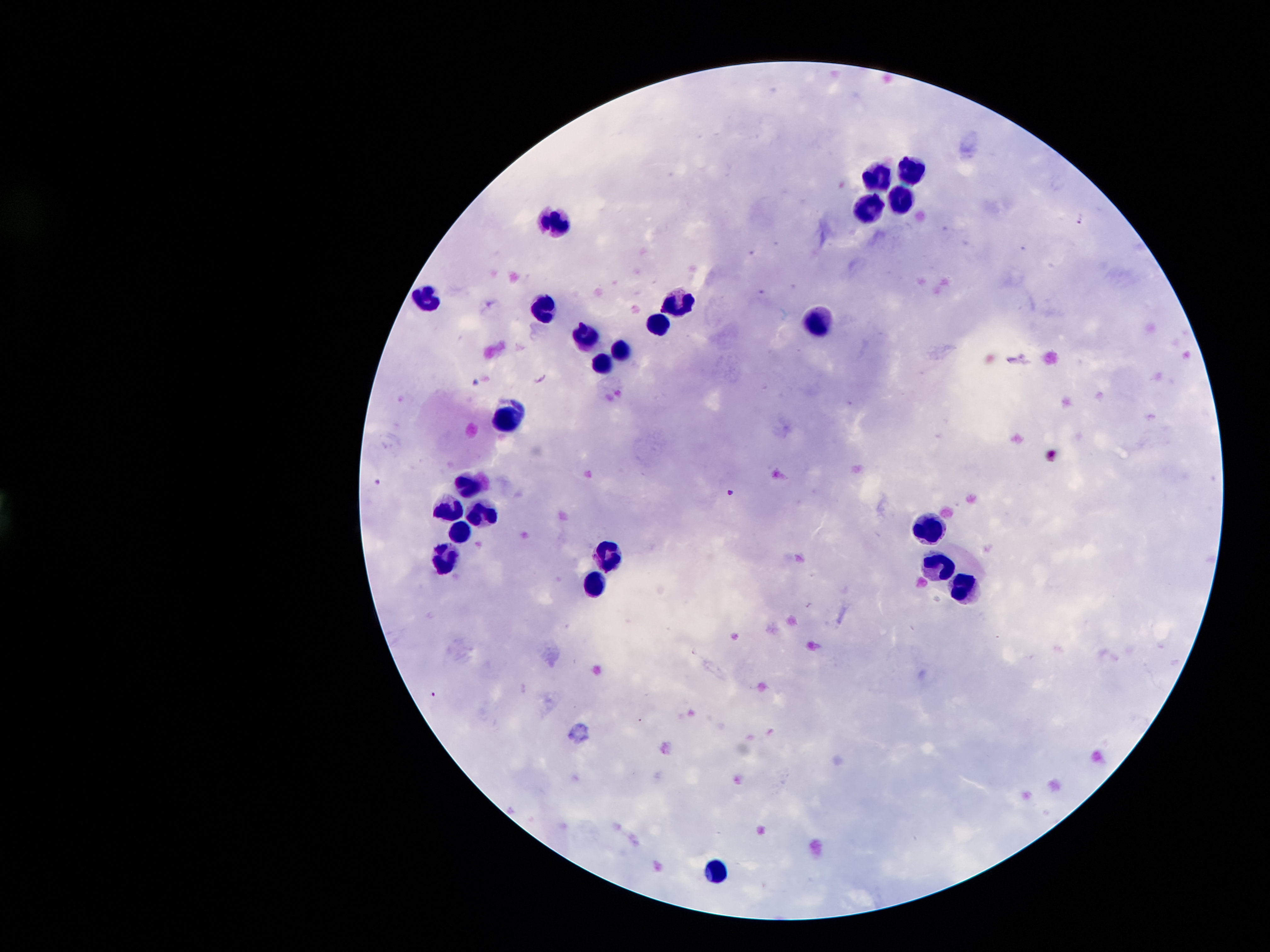

coordinate format = approximate object centers, in pixels from the top-left corner
malaria parasite locations = (x=1080, y=220), (x=377, y=482), (x=730, y=492), (x=434, y=693)
leukocyte locations = (x=874, y=170), (x=915, y=170), (x=865, y=203), (x=896, y=203), (x=552, y=217), (x=434, y=296), (x=676, y=299), (x=543, y=310), (x=814, y=320), (x=656, y=322), (x=582, y=333), (x=619, y=350), (x=602, y=366), (x=512, y=419), (x=467, y=480), (x=445, y=510), (x=483, y=514), (x=461, y=529), (x=927, y=531), (x=610, y=556), (x=445, y=558), (x=942, y=567), (x=597, y=589), (x=968, y=594), (x=713, y=866)
capture = smartphone through the microscope eyepiece
image size = 1270×952 pixels
patient malaria status = infected with Plasmodium falciparum
magnification = 100x
field of view = single
stain = Giemsa
preparation = thick blood film